Name the blood parasite species.
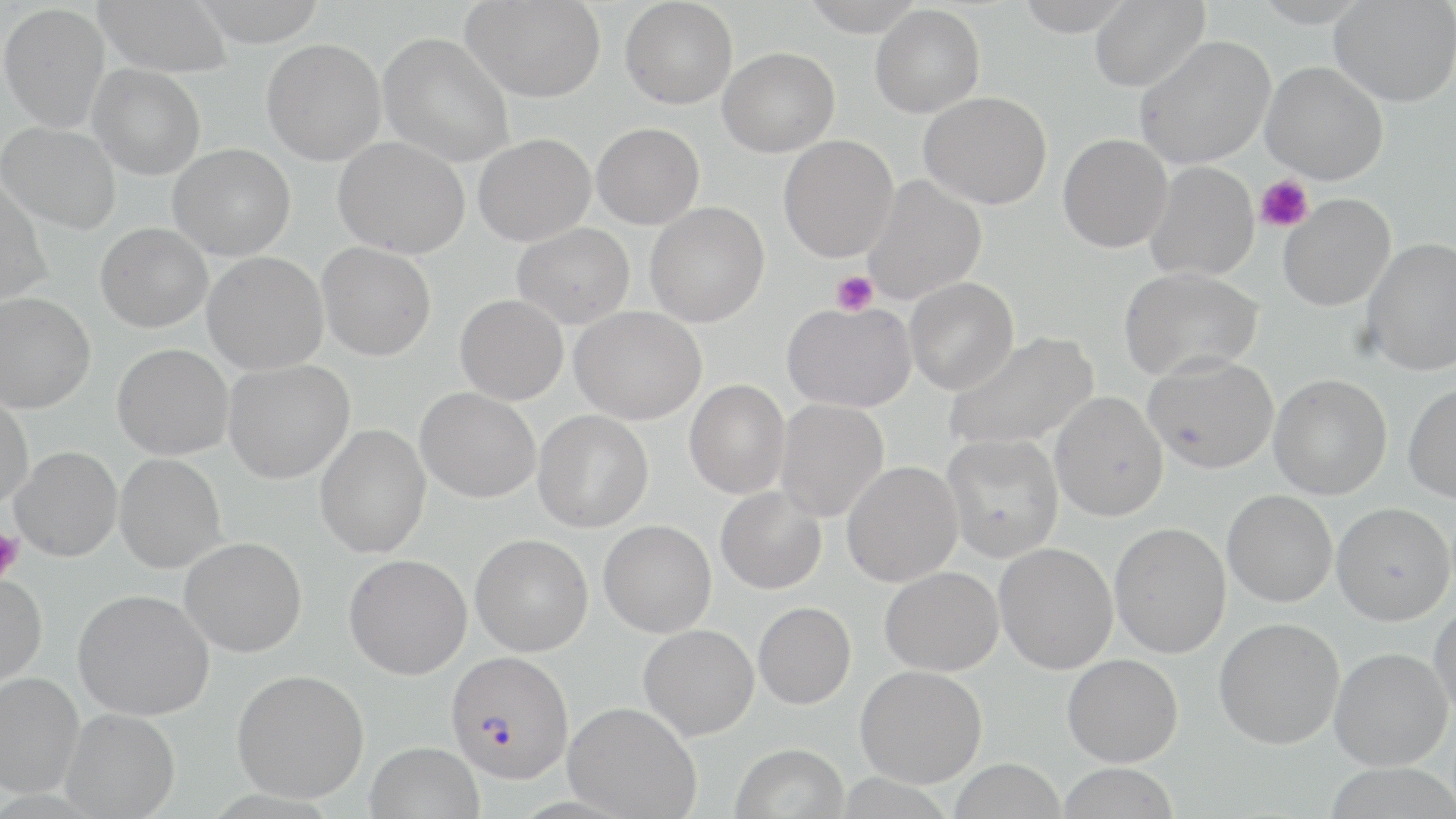

Plasmodium falciparum.

Approximate bounding boxes as [x1, y1, x2, y2] in pixels. Plasmodium falciparum-infected red blood cell locations: [445, 650, 574, 783]. Platelet locations: [1255, 174, 1313, 233], [831, 270, 878, 315], [0, 527, 23, 585]. Uninfected red blood cell locations: [94, 0, 232, 77], [191, 0, 328, 48], [461, 0, 606, 102], [620, 0, 738, 109], [801, 0, 927, 36], [1013, 0, 1135, 36], [1089, 0, 1210, 92], [1329, 0, 1455, 107], [0, 3, 110, 133], [870, 4, 985, 118], [378, 32, 514, 167], [1135, 35, 1276, 169], [261, 39, 386, 165], [718, 47, 839, 157], [1260, 61, 1388, 184], [88, 64, 205, 180], [918, 91, 1052, 209], [1, 122, 121, 234], [591, 122, 705, 229], [473, 133, 596, 246], [1058, 133, 1173, 253], [778, 135, 898, 262], [332, 137, 469, 259], [168, 143, 295, 261], [1145, 161, 1260, 282], [861, 175, 986, 304], [0, 176, 52, 306], [1278, 193, 1396, 312], [644, 202, 769, 327], [95, 222, 212, 333], [512, 223, 635, 329], [1362, 238, 1456, 375], [316, 241, 436, 361], [202, 252, 328, 375], [1117, 266, 1263, 382], [905, 277, 1019, 395], [0, 292, 96, 414], [455, 294, 568, 405], [782, 301, 917, 413], [570, 306, 706, 425], [945, 331, 1098, 454], [112, 343, 233, 460], [1142, 353, 1278, 474], [223, 359, 354, 484], [1269, 373, 1392, 500], [685, 379, 790, 499], [1403, 382, 1456, 503], [416, 388, 540, 503], [1049, 392, 1168, 521], [0, 394, 33, 510], [775, 398, 888, 522], [533, 409, 653, 532], [314, 424, 430, 558], [941, 434, 1065, 563], [10, 446, 123, 562], [114, 453, 227, 573], [842, 461, 964, 588], [715, 487, 826, 594], [1222, 489, 1337, 607], [1331, 502, 1455, 625], [599, 520, 716, 638], [1109, 522, 1231, 659], [470, 534, 593, 656], [179, 537, 307, 657], [994, 542, 1118, 674], [344, 553, 472, 680], [879, 567, 1003, 676], [0, 573, 47, 688], [72, 589, 214, 721], [1429, 598, 1456, 720], [753, 601, 856, 710], [1213, 616, 1345, 750], [638, 623, 759, 741], [1329, 646, 1452, 770], [1062, 653, 1183, 767], [855, 664, 987, 788], [232, 669, 369, 803], [0, 672, 83, 799], [563, 702, 701, 819], [61, 708, 180, 818], [365, 741, 485, 819], [731, 743, 849, 819], [949, 758, 1067, 818], [1057, 762, 1181, 819]. Light microscopy. May-Grünwald-Giemsa-stained preparation. Single field of view. Thin blood film. Captured at 1000x magnification. Image is 1456×819 pixels.